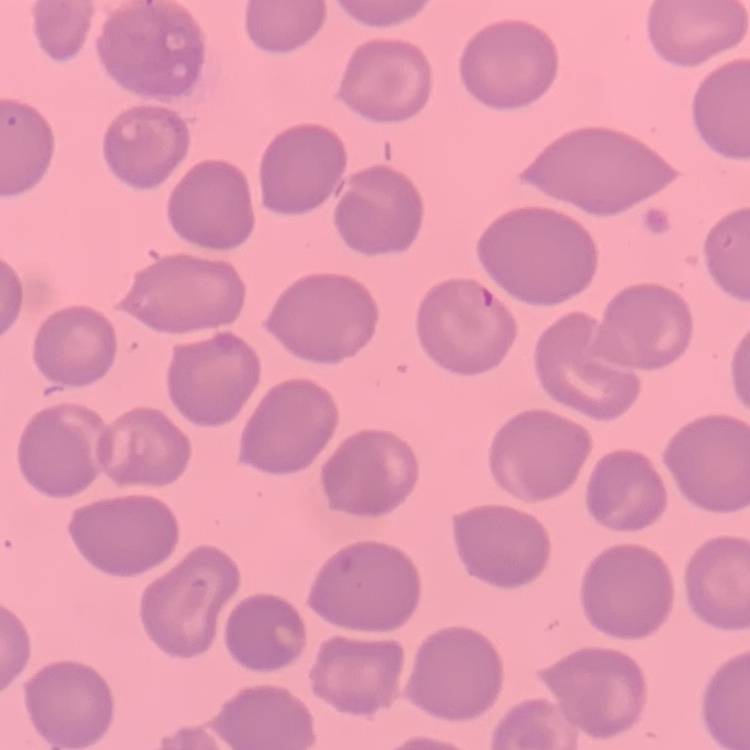
Summary:
  - Red blood cell morphology: no rouleaux formation
  - Preparation: thin peripheral smear
  - Image type: square crop of a larger photomicrograph
  - Stain: Field's or Giemsa